Report the malaria status of this cell.
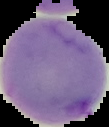

Uninfected.

Summary:
  - Image size: 109×127 pixels
  - Preparation: thin blood film
  - Image type: segmented cell region on a black background